Identify the parasite.
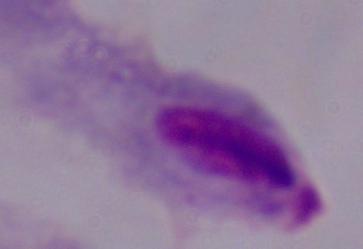
A trichomonad.

Summary:
  - Modality: photomicrograph
  - Magnification: 1000x